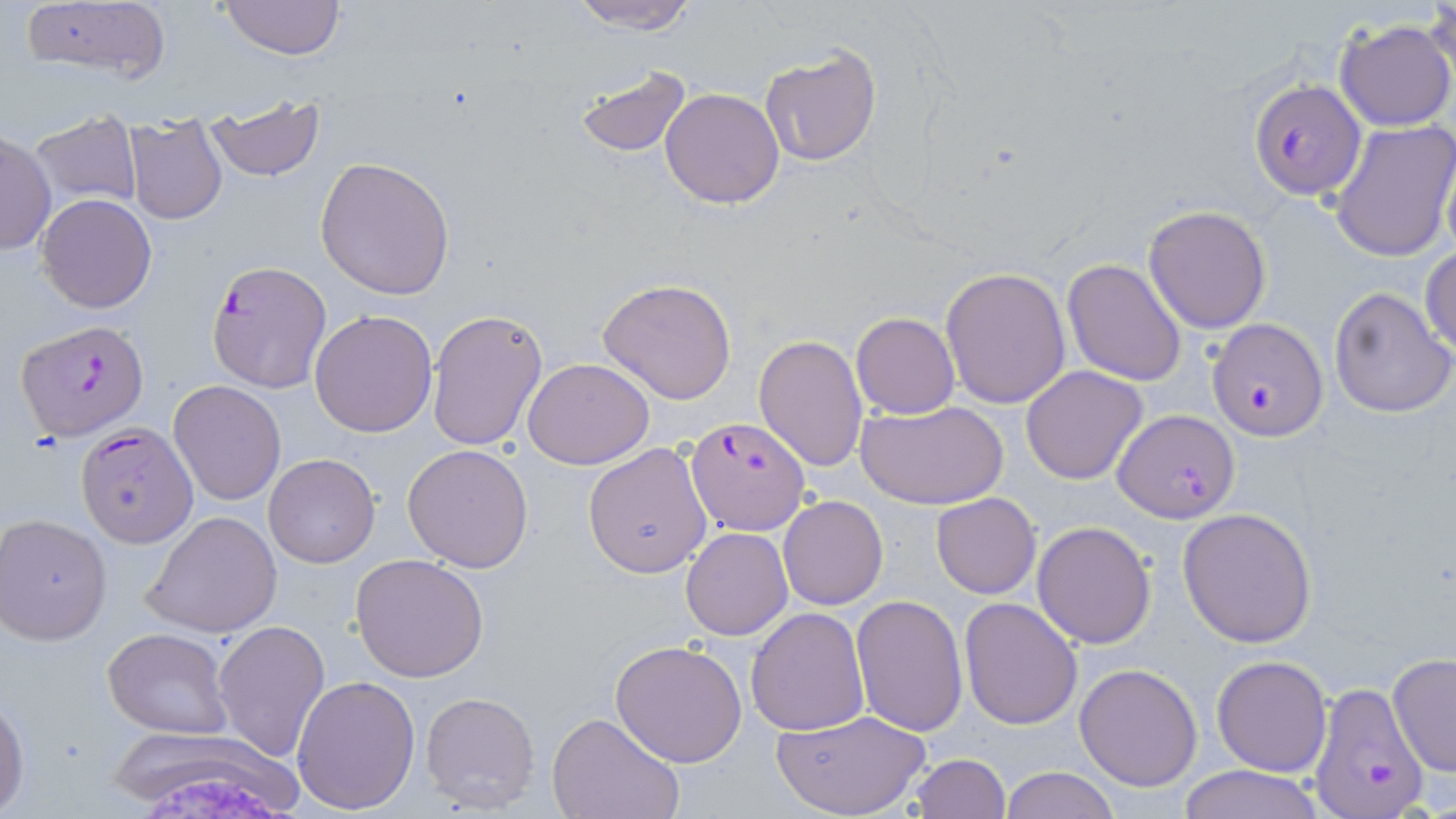
Summary:
  - Coordinate format: approximate bounding boxes as named x1/y1/x2/y2 corners in pixels
  - Uninfected red blood cell locations: (x1=564, y1=0, x2=702, y2=34), (x1=217, y1=1, x2=347, y2=59), (x1=17, y1=2, x2=171, y2=88), (x1=1421, y1=5, x2=1456, y2=99), (x1=1335, y1=18, x2=1455, y2=132), (x1=760, y1=46, x2=883, y2=167), (x1=571, y1=63, x2=693, y2=158), (x1=660, y1=88, x2=784, y2=209), (x1=203, y1=100, x2=326, y2=182), (x1=27, y1=110, x2=145, y2=210), (x1=125, y1=118, x2=227, y2=225), (x1=1329, y1=118, x2=1456, y2=261), (x1=0, y1=129, x2=54, y2=256), (x1=315, y1=155, x2=457, y2=301), (x1=36, y1=193, x2=156, y2=312), (x1=1143, y1=204, x2=1272, y2=333), (x1=1421, y1=247, x2=1456, y2=357), (x1=1062, y1=257, x2=1187, y2=387), (x1=939, y1=266, x2=1071, y2=410), (x1=595, y1=277, x2=739, y2=405), (x1=1329, y1=287, x2=1455, y2=416), (x1=425, y1=309, x2=547, y2=453), (x1=309, y1=310, x2=437, y2=437), (x1=850, y1=312, x2=960, y2=419), (x1=754, y1=334, x2=869, y2=473), (x1=523, y1=357, x2=655, y2=469), (x1=1021, y1=365, x2=1148, y2=484), (x1=169, y1=380, x2=286, y2=504), (x1=858, y1=399, x2=1007, y2=510), (x1=583, y1=441, x2=714, y2=578), (x1=402, y1=443, x2=534, y2=572), (x1=263, y1=454, x2=380, y2=569), (x1=931, y1=493, x2=1040, y2=599), (x1=778, y1=494, x2=888, y2=610), (x1=1175, y1=507, x2=1317, y2=648), (x1=141, y1=511, x2=282, y2=638), (x1=1, y1=514, x2=114, y2=646), (x1=1033, y1=520, x2=1156, y2=650), (x1=681, y1=527, x2=792, y2=640), (x1=351, y1=554, x2=491, y2=682), (x1=852, y1=595, x2=969, y2=735), (x1=959, y1=597, x2=1082, y2=730), (x1=746, y1=608, x2=871, y2=736), (x1=212, y1=620, x2=330, y2=763), (x1=103, y1=627, x2=233, y2=740), (x1=609, y1=640, x2=749, y2=768), (x1=1387, y1=653, x2=1456, y2=775), (x1=1210, y1=654, x2=1332, y2=776), (x1=1074, y1=663, x2=1203, y2=792), (x1=292, y1=675, x2=421, y2=815), (x1=420, y1=689, x2=542, y2=814), (x1=0, y1=693, x2=28, y2=812), (x1=775, y1=710, x2=930, y2=819), (x1=546, y1=713, x2=683, y2=819), (x1=106, y1=732, x2=312, y2=806), (x1=908, y1=753, x2=1011, y2=819), (x1=1177, y1=765, x2=1324, y2=819), (x1=999, y1=766, x2=1120, y2=819)
  - Plasmodium falciparum-infected red blood cell locations: (x1=1248, y1=80, x2=1367, y2=201), (x1=208, y1=260, x2=331, y2=393), (x1=16, y1=319, x2=148, y2=441), (x1=1206, y1=319, x2=1327, y2=440), (x1=1112, y1=410, x2=1239, y2=522), (x1=685, y1=413, x2=810, y2=537), (x1=74, y1=423, x2=197, y2=547), (x1=1310, y1=684, x2=1429, y2=819)
  - Slide-level diagnosis: Plasmodium falciparum
  - Preparation: thin blood smear
  - Magnification: 1000x
  - Field of view: single
  - Image size: 1456×819 pixels
  - Modality: light microscopy
  - Stain: May-Grünwald-Giemsa